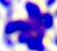
Captured at 400x magnification. A leukocyte is shown. Micrograph.